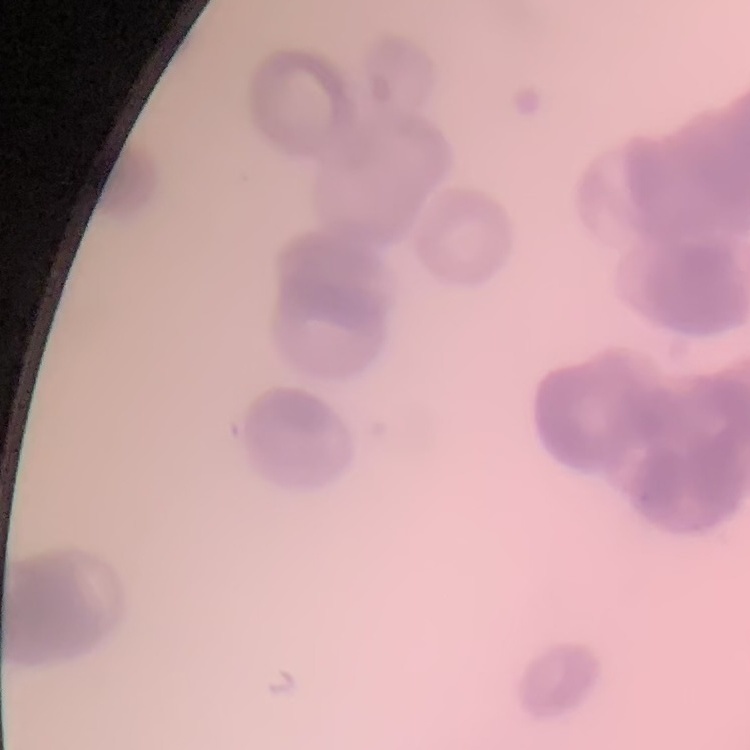
{
  "erythrocyte_morphology": "rouleaux formation",
  "image_type": "one tile cut from a larger photomicrograph",
  "preparation": "thin blood smear",
  "stain": "Field's or Giemsa"
}